Comment on the morphology of the erythrocytes.
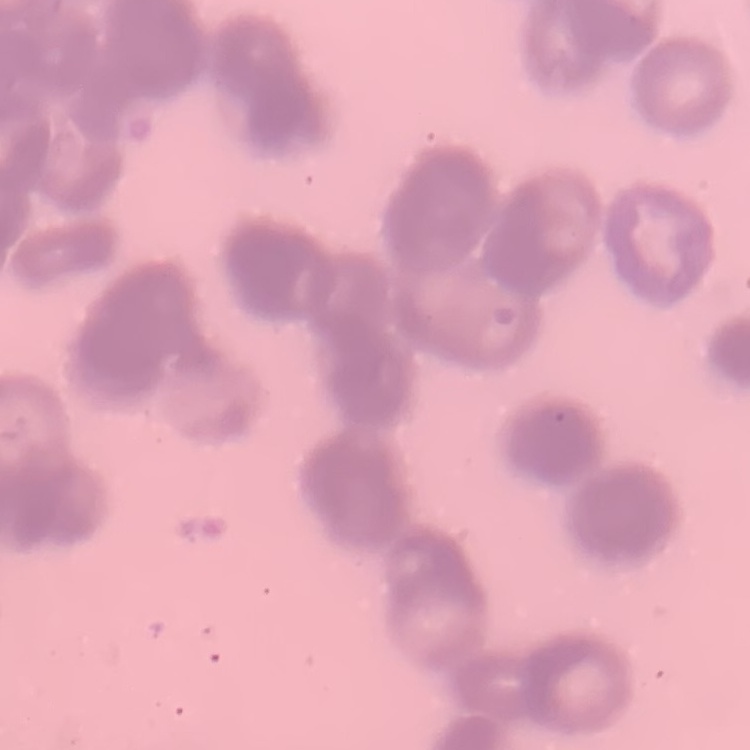

Rouleaux formation.

stain: Field's or Giemsa
preparation: thin blood film
image_type: square crop of a larger photomicrograph